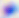
identification = Toxoplasma gondii
modality = micrograph
magnification = 400x